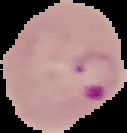
Malaria status: parasitized. Cell region segmented out of the field of view; the surrounding area is masked to black. From a thin blood smear. Image is 127×133 pixels.